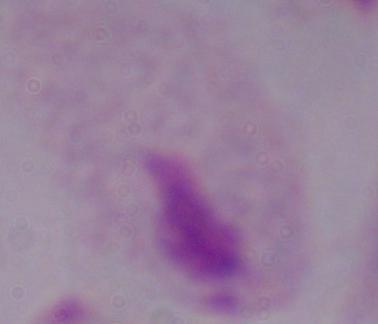

Summary:
  - Magnification: 1000x
  - Modality: micrograph
  - Identification: trichomonad